Give the position of every malaria parasite.
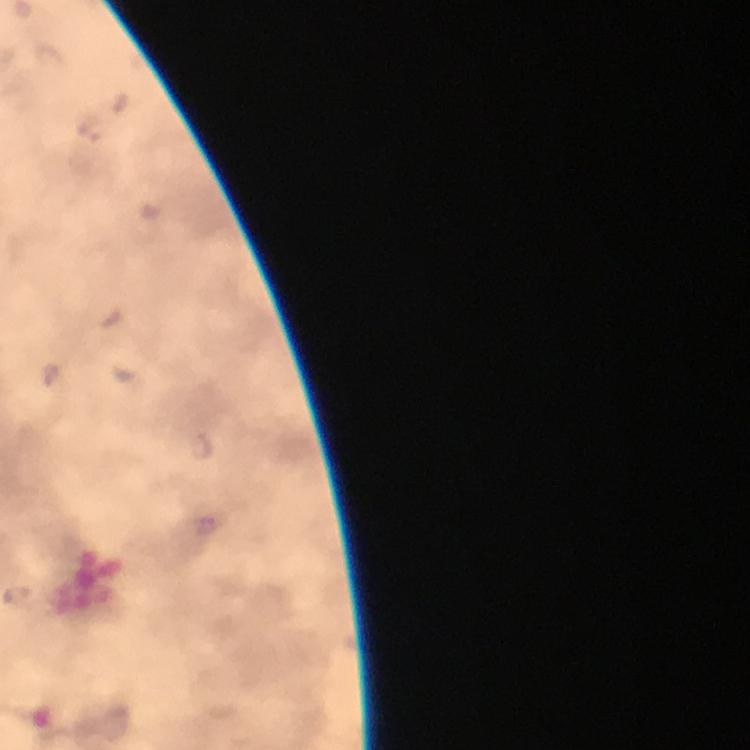
Approximate object centers, in pixels from the top-left corner.
Malaria parasites: (x=92, y=129), (x=202, y=446).

image size = 750×750 pixels
immersion oil = applied
stain = Giemsa
capture = smartphone camera through the microscope
magnification = 100x
preparation = thick smear
cropped from = a single field of view
context = from a diagnostic examination for malaria